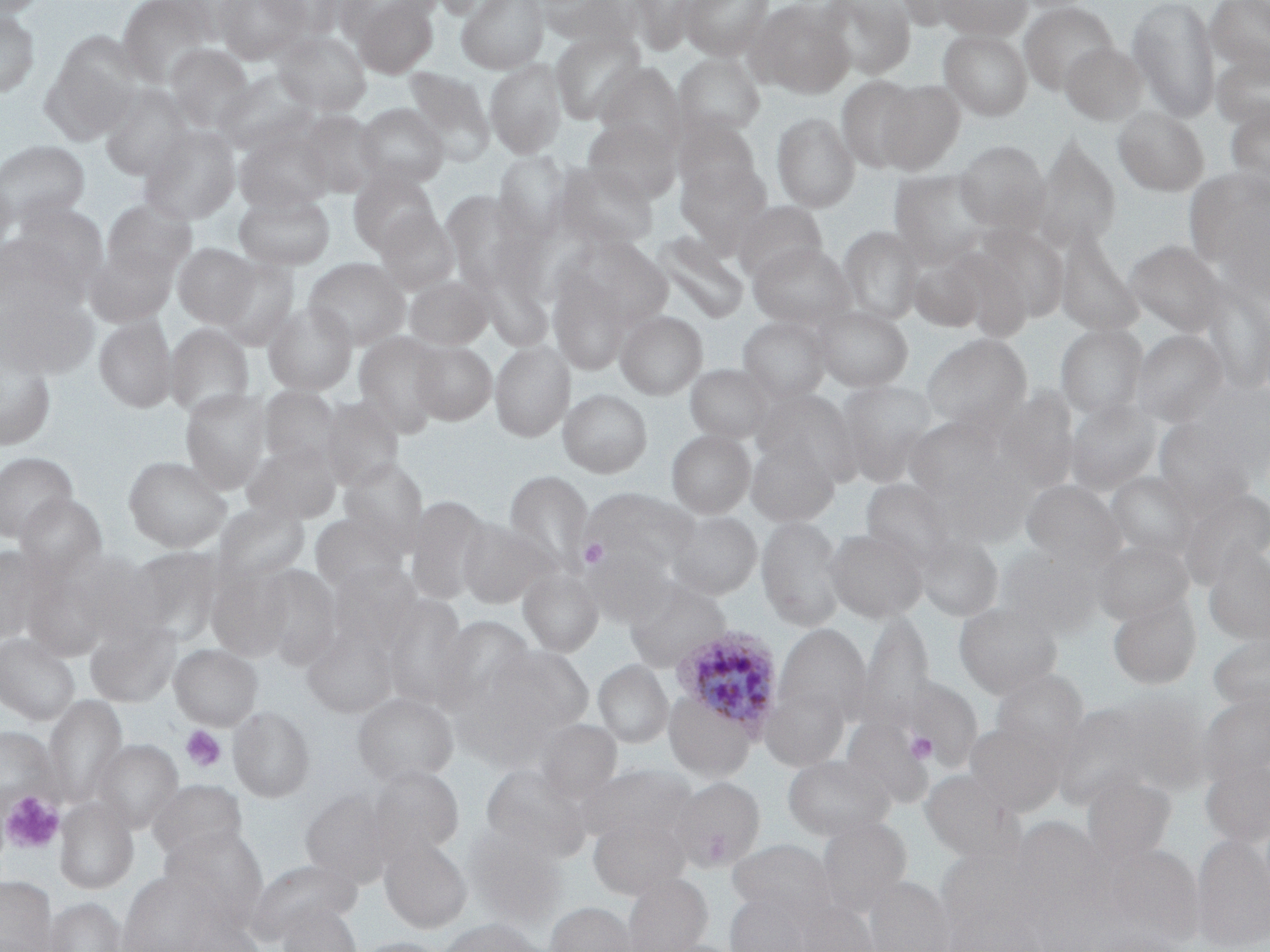 Approximate bounding boxes as (x1,y1)-(x2,y2) corner pairs in pixels. Uninfected red blood cell locations: (1,0)-(48,19), (116,0)-(217,88), (215,0)-(310,64), (261,0)-(352,39), (351,0)-(440,78), (431,0)-(517,21), (457,0)-(549,73), (533,0)-(637,45), (625,0)-(702,55), (679,0)-(775,60), (816,0)-(915,80), (891,0)-(979,29), (934,0)-(1032,40), (1127,0)-(1220,121), (1205,0)-(1270,79), (748,1)-(854,97), (1019,2)-(1118,94), (0,9)-(39,99), (551,29)-(646,123), (939,30)-(1032,121), (54,31)-(145,113), (273,31)-(371,116), (288,32)-(375,199), (1060,41)-(1146,125), (165,44)-(254,131), (1211,47)-(1270,132), (41,52)-(136,144), (674,53)-(765,139), (485,59)-(567,158), (596,62)-(686,154), (403,66)-(495,165), (215,69)-(315,154), (836,76)-(922,172), (876,79)-(965,173), (99,84)-(194,180), (1225,101)-(1270,193), (355,102)-(449,188), (1112,106)-(1209,196), (298,110)-(383,197), (772,112)-(860,212), (674,116)-(760,198), (583,117)-(680,203), (139,124)-(241,224), (235,129)-(334,213), (1032,137)-(1121,251), (0,138)-(92,229), (954,140)-(1049,232), (494,151)-(570,238), (675,159)-(771,251), (556,162)-(658,250), (1184,167)-(1270,272), (888,168)-(991,266), (348,171)-(438,255), (0,174)-(16,261), (441,190)-(533,290), (234,192)-(334,270), (102,199)-(196,279), (8,201)-(109,288), (734,201)-(828,283), (374,209)-(459,292), (838,225)-(923,324), (974,225)-(1069,324), (1055,229)-(1143,338), (653,232)-(748,323), (0,233)-(84,319), (557,235)-(671,338), (1124,240)-(1226,337), (748,242)-(855,328), (173,243)-(259,327), (86,245)-(178,327), (909,250)-(991,332), (303,257)-(410,350), (216,258)-(299,350), (548,269)-(634,375), (404,274)-(493,350), (1197,277)-(1269,394), (1,291)-(95,378), (263,301)-(357,396), (813,304)-(913,391), (616,310)-(707,398), (94,315)-(177,412), (739,315)-(830,402), (164,323)-(254,419), (1055,323)-(1147,418), (1131,329)-(1228,426), (354,331)-(446,436), (921,333)-(1032,432), (411,340)-(496,424), (490,341)-(574,441), (0,343)-(56,451), (686,363)-(772,443), (835,379)-(938,485), (258,385)-(342,468), (180,387)-(272,493), (558,388)-(652,477), (755,388)-(861,483), (991,389)-(1078,487), (319,395)-(404,491), (1066,398)-(1161,494), (904,414)-(1004,498), (1153,420)-(1249,507), (666,429)-(755,518), (746,437)-(839,527), (244,441)-(342,523), (0,451)-(78,541), (123,455)-(231,552), (339,458)-(428,550), (504,470)-(593,574), (1105,471)-(1198,561), (861,478)-(959,569), (1021,480)-(1123,569), (579,487)-(698,578), (1179,489)-(1270,586), (14,494)-(107,577), (406,494)-(491,606), (213,500)-(310,585), (666,509)-(762,600), (309,511)-(408,594), (756,514)-(846,631), (458,518)-(553,609), (824,526)-(928,622), (916,532)-(1002,622), (1092,538)-(1193,626), (582,543)-(674,626), (0,544)-(58,643), (1202,545)-(1270,644), (125,546)-(226,642), (996,546)-(1100,636), (68,551)-(161,640), (324,561)-(422,660), (254,565)-(342,667), (206,566)-(293,660), (518,567)-(603,656), (22,572)-(108,660), (623,576)-(731,673), (378,593)-(471,708), (1107,593)-(1201,690), (954,600)-(1063,699), (855,611)-(935,733), (433,615)-(535,711), (85,618)-(180,707), (774,623)-(871,729), (302,625)-(399,719), (1208,630)-(1270,717), (0,633)-(81,725), (169,643)-(262,730), (486,644)-(595,735), (593,659)-(672,748), (991,669)-(1088,762), (896,674)-(983,772), (759,680)-(850,771), (1100,688)-(1211,793), (664,691)-(757,781), (352,692)-(458,786), (1197,692)-(1270,783), (44,694)-(128,806), (1052,702)-(1164,807), (228,705)-(315,802), (842,717)-(932,809), (534,719)-(622,803), (964,721)-(1067,815), (0,727)-(57,812), (93,740)-(182,832), (782,753)-(895,841), (1200,759)-(1270,847), (580,763)-(695,844), (366,764)-(464,858), (481,764)-(587,857), (920,769)-(1023,863), (1082,775)-(1176,864), (671,776)-(765,870), (147,779)-(248,863), (300,788)-(394,886), (55,795)-(138,894), (588,814)-(690,899), (816,816)-(911,917), (1011,817)-(1106,908), (160,825)-(269,920), (464,827)-(567,926), (1192,833)-(1269,951), (380,837)-(471,933), (727,839)-(837,924), (1103,843)-(1204,946), (935,848)-(1045,948), (244,857)-(361,943), (117,871)-(219,952), (622,871)-(712,952), (863,875)-(954,952), (0,876)-(58,951), (724,892)-(813,952), (42,896)-(129,952), (791,899)-(878,952), (546,901)-(637,952), (276,902)-(361,952), (182,916)-(264,952), (436,918)-(544,952), (1087,929)-(1194,952), (350,937)-(452,952). Plasmodium ovale-infected red blood cell locations: (672,625)-(784,738). Platelet locations: (579,538)-(608,568), (181,725)-(227,773), (905,731)-(937,764), (2,792)-(64,853). Slide-level diagnosis: Plasmodium ovale. May-Grünwald-Giemsa-stained preparation. Image is 1270×952 pixels. One field of a larger specimen. Thin blood smear. Light microscopy. 1000x magnification.